Give the extent of all Plasmodium falciparum-infected red blood cells.
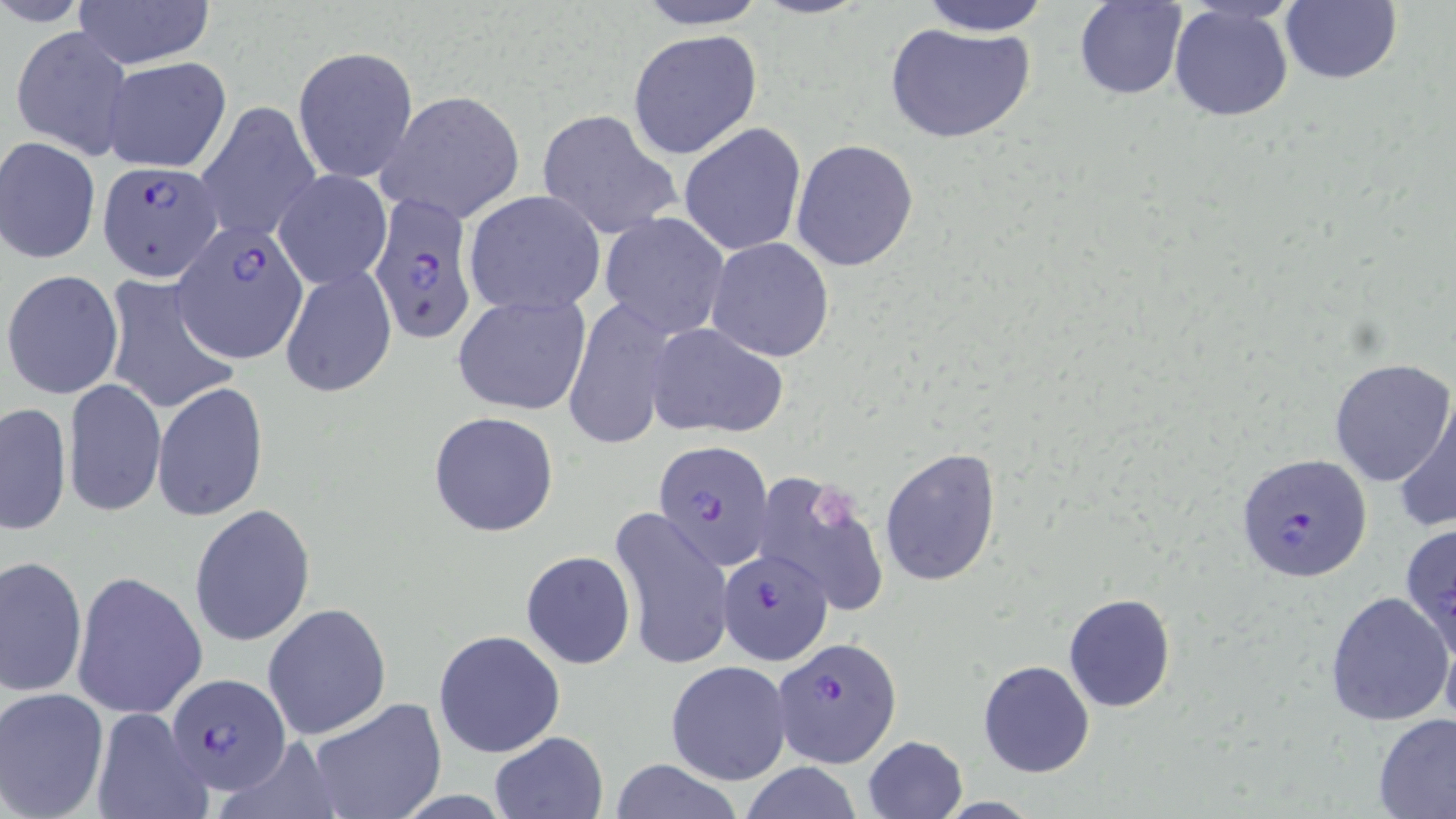
Approximate bounding boxes as [x1, y1, x2, y2] in pixels.
Plasmodium falciparum-infected red blood cells: [97, 155, 223, 275], [370, 194, 481, 347], [172, 225, 310, 362], [653, 440, 776, 571], [1237, 452, 1372, 585], [718, 547, 834, 666], [773, 639, 901, 768], [165, 673, 292, 794].

slide-level diagnosis = Plasmodium falciparum
modality = optical microscopy
magnification = 1000x
uninfected red blood cell locations = approximate bounding boxes as [x1, y1, x2, y2] in pixels: [71, 0, 216, 69], [627, 0, 773, 30], [752, 0, 870, 20], [1280, 0, 1401, 85], [1, 1, 93, 29], [915, 1, 1054, 36], [1073, 1, 1187, 100], [1168, 4, 1295, 122], [882, 22, 1036, 144], [10, 25, 134, 161], [627, 29, 763, 160], [292, 44, 419, 185], [102, 57, 233, 174], [377, 89, 525, 224], [194, 100, 322, 242], [537, 109, 681, 240], [678, 122, 807, 257], [1, 136, 101, 264], [790, 138, 920, 271], [274, 170, 391, 290], [463, 189, 608, 314], [598, 211, 731, 339], [706, 236, 834, 362], [280, 265, 397, 397], [3, 270, 124, 400], [101, 277, 241, 415], [452, 293, 592, 416], [560, 301, 678, 450], [645, 322, 789, 440], [1328, 356, 1454, 486], [63, 378, 165, 517], [153, 383, 268, 522], [1394, 389, 1456, 534], [2, 402, 72, 535], [428, 410, 561, 538], [880, 446, 1001, 588], [753, 468, 892, 622], [188, 503, 316, 649], [610, 507, 733, 671], [1399, 522, 1456, 657], [521, 550, 635, 669], [1, 553, 87, 701], [70, 572, 208, 720], [1324, 589, 1452, 727], [1062, 592, 1176, 713], [262, 603, 391, 742], [1440, 623, 1456, 737], [433, 629, 566, 759], [666, 660, 790, 785], [978, 660, 1095, 779], [0, 689, 109, 818], [305, 697, 447, 819], [90, 707, 214, 818], [1373, 712, 1456, 817], [489, 731, 610, 817], [862, 735, 968, 819], [608, 759, 745, 819], [739, 763, 866, 819]
image size = 1456×819 pixels
field of view = one of a larger specimen
preparation = thin blood film
stain = May-Grünwald-Giemsa
platelet locations = approximate bounding boxes as [x1, y1, x2, y2] in pixels: [811, 484, 861, 532]